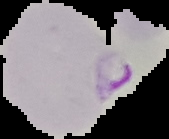
Summary:
  - Preparation: thin blood smear
  - Image type: segmented cell region with the area outside set to black
  - Image size: 169×139 pixels
  - Malaria status: parasitized